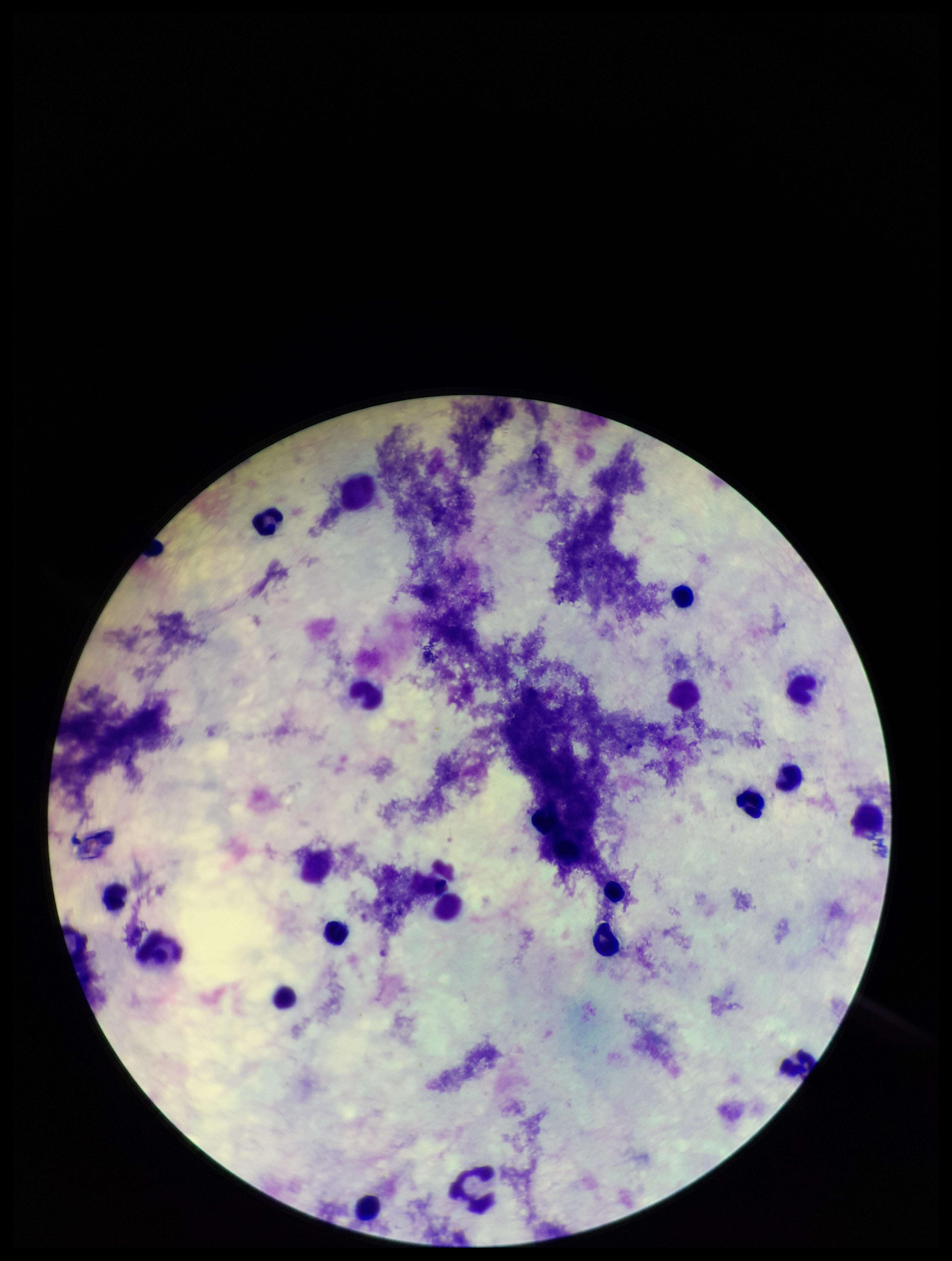

Summary:
  - Image size: 952×1261 pixels
  - Preparation: thick
  - Patient malaria status: negative
  - Stain: Giemsa
  - Parasite count: 0
  - Plasmodium parasites: none detected
  - Capture: smartphone photograph through the microscope eyepiece
  - Field of view: one from this slide
  - Leukocyte count: 21